Evaluate for parasitized red blood cells.
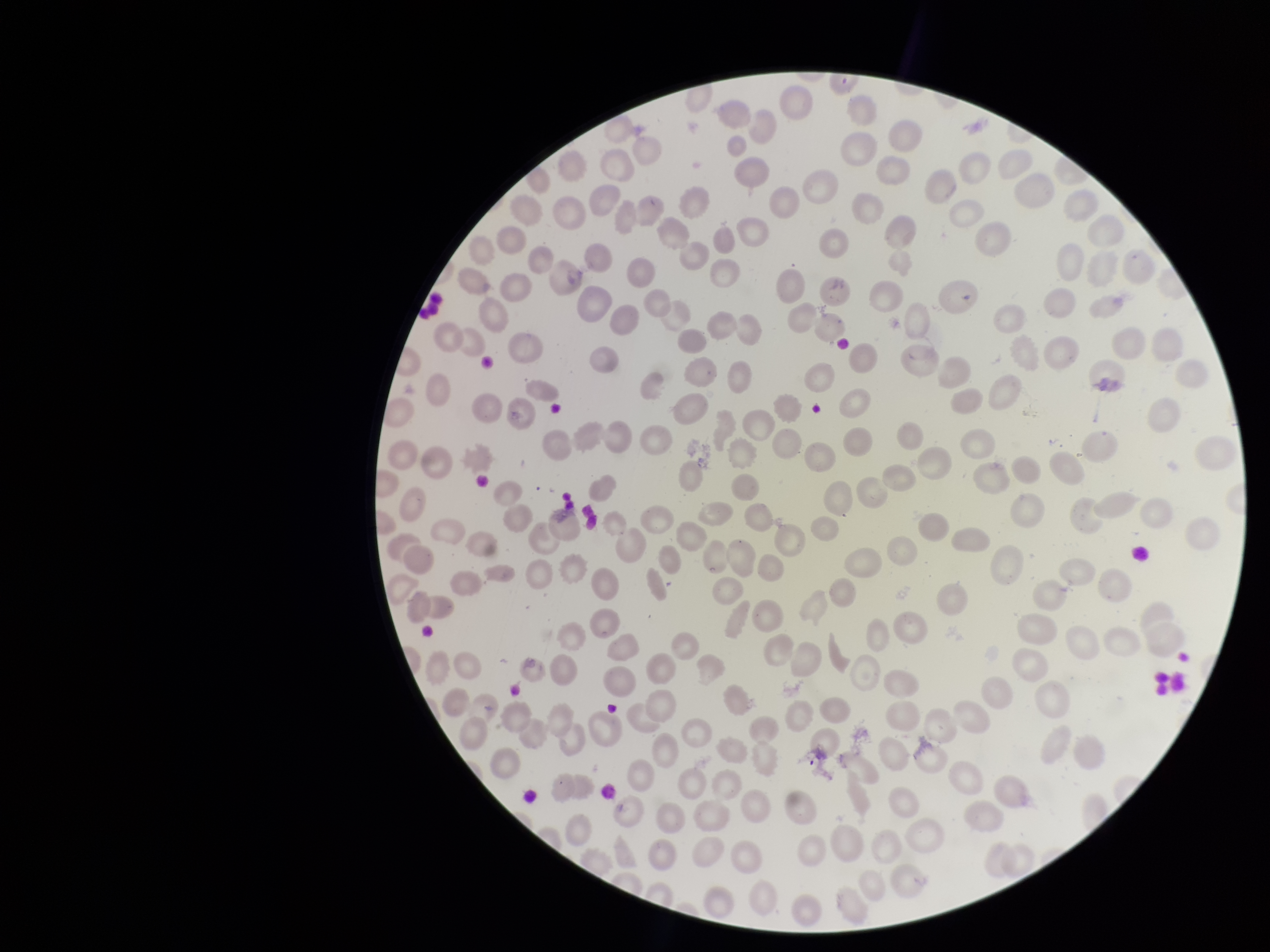
None seen.

Summary:
  - Patient malaria status: infected
  - Red blood cell count: 178
  - Preparation: thin
  - Field of view: one from this slide
  - Capture: smartphone photograph through the microscope eyepiece
  - Parasitized red blood cell count: 0
  - Stain: Giemsa
  - Species reported for this patient: Plasmodium falciparum
  - Image size: 1270×952 pixels